Name the parasite shown.
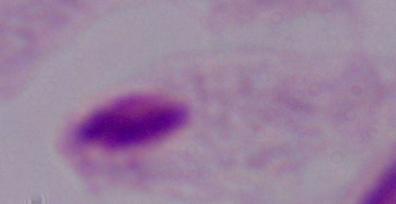

This is a trichomonad.

{
  "modality": "photomicrograph",
  "magnification": "1000x"
}